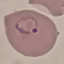

result: malaria parasites identified
image_type: automatically extracted cell patch, resized to 64 × 64 pixels
stain: Giemsa
preparation: thin blood film
capture: smartphone camera at the microscope eyepiece